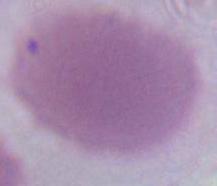

identification = erythrocyte
modality = micrograph
magnification = 1000x